Classify this cell by malaria status.
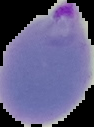
Parasitized.

From a thin blood smear. Image is 94×127 pixels. Segmented cell region on a black background.